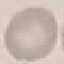

result = no malaria parasites seen
capture = smartphone through the microscope eyepiece
preparation = thin smear
image type = automatically extracted cell patch, resized to 64 × 64 pixels
stain = Giemsa